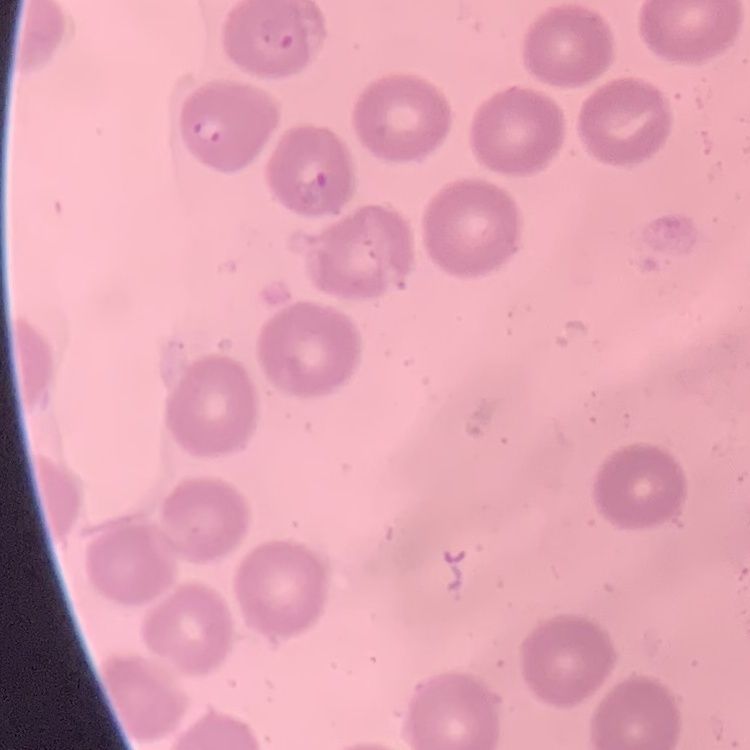

The red blood cells show no rouleaux formation. Field's or Giemsa stain. Thin blood film. Square crop of a larger photomicrograph.